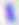

Captured at 400x magnification. Toxoplasma gondii is seen. Micrograph.